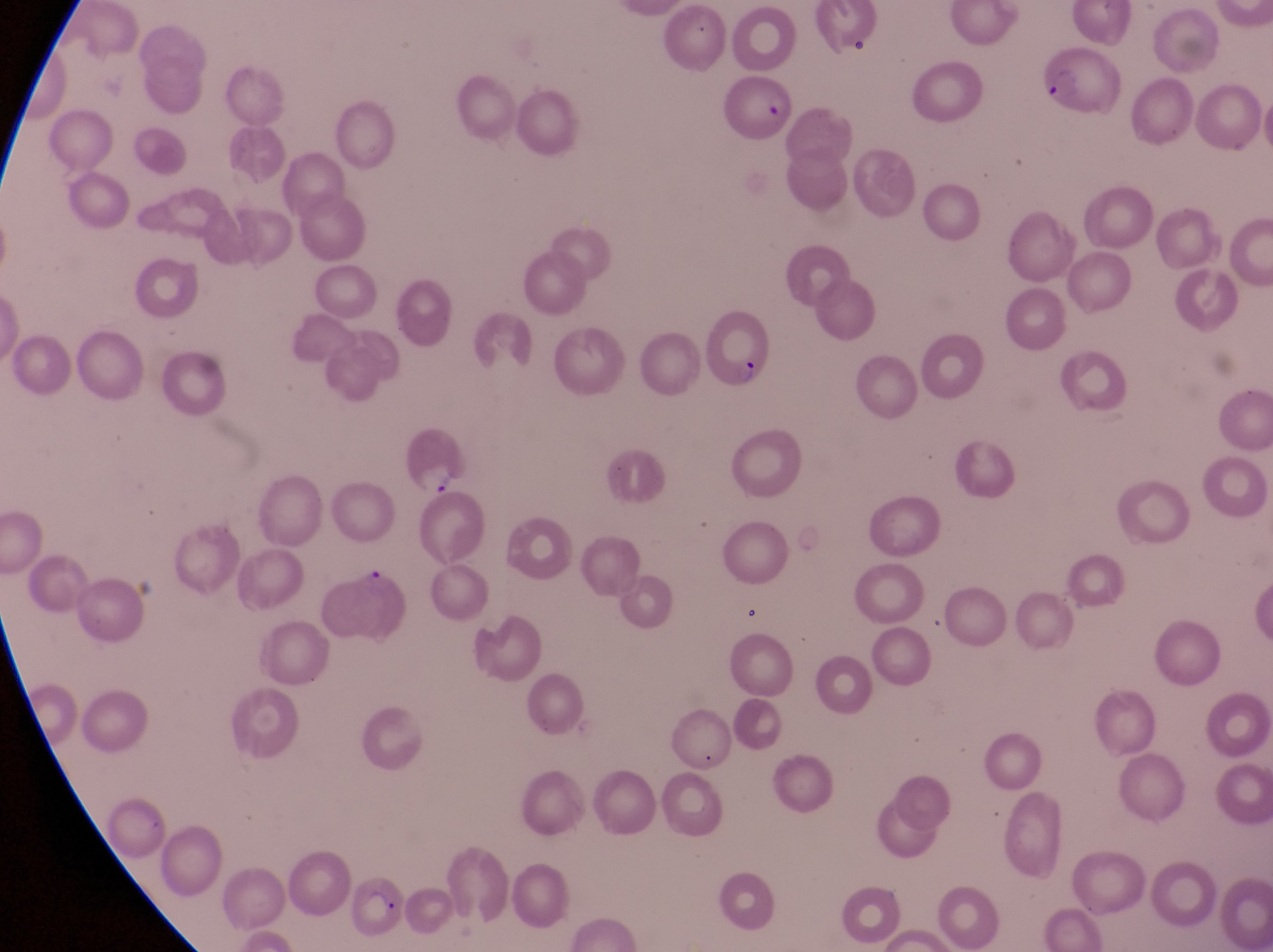

Approximate bounding boxes as {left, top, right, bottom} in pixels.
Summary:
  - Parasitised red blood cell locations: {1031, 50, 1124, 120}, {717, 74, 795, 139}, {704, 313, 784, 396}
  - Artifact (platelet-like body, stain precipitate, or debris) locations: {844, 25, 876, 62}, {429, 464, 469, 501}
  - Field of view: single
  - Preparation: thin blood film
  - Image size: 1273×952 pixels
  - Magnification: 1000x
  - Capture: smartphone photograph through the eyepiece of an Olympus CX-23 microscope
  - Country: Uganda